Identify the parasite.
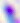

Toxoplasma gondii.

magnification = 400x
modality = micrograph